Assess the morphology of the erythrocytes.
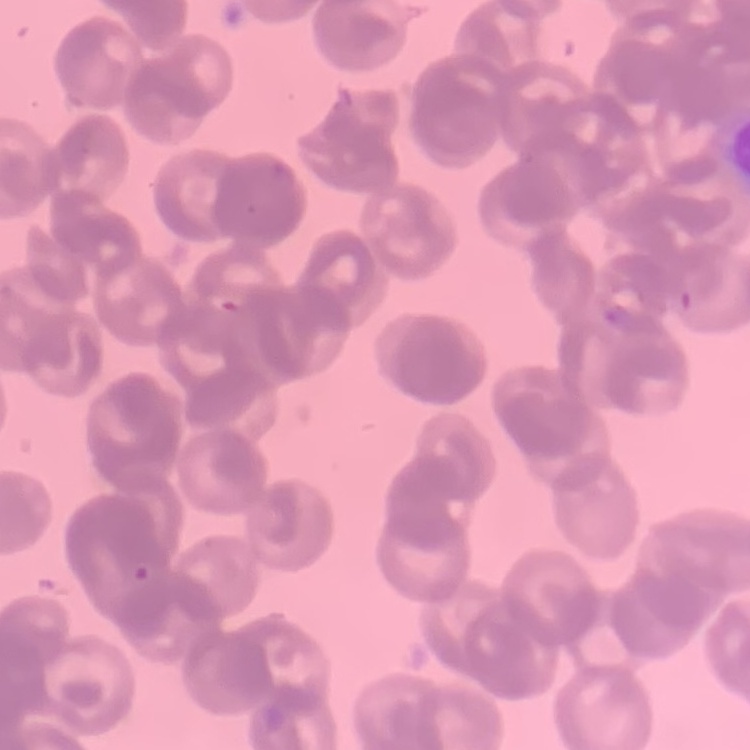

They show rouleaux formation.

Stained with either Field's or Giemsa. Square crop of a larger photomicrograph. Thin peripheral smear.